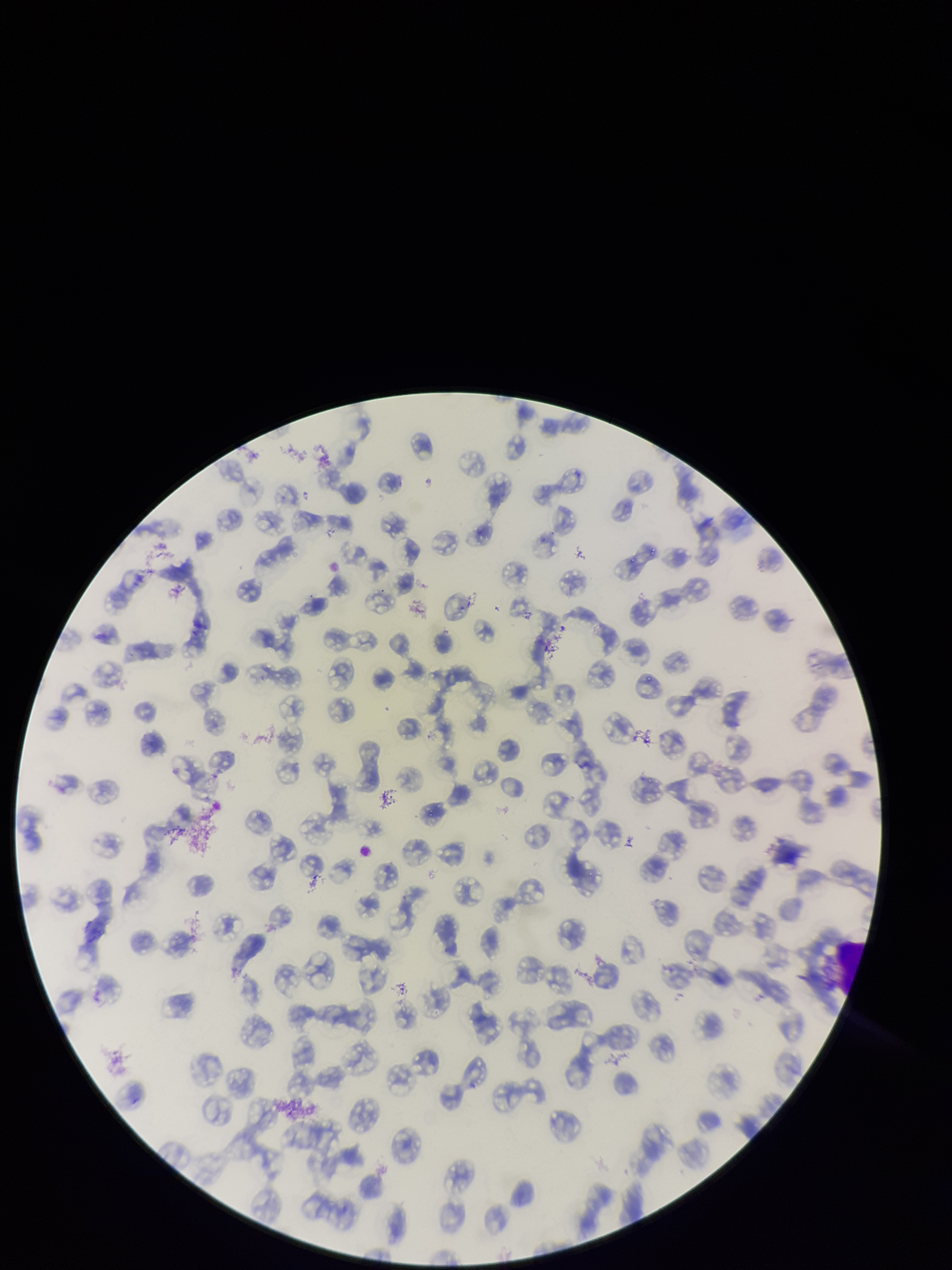

image size = 952×1270 pixels
parasitized red blood cells = none seen
stain = Giemsa
parasitized red blood cell count = 0
capture = smartphone photograph through the microscope eyepiece
preparation = thin smear
patient malaria status = infected
field of view = one from this slide
red blood cell count = 155
species reported for this patient = Plasmodium falciparum